State the blood parasite species.
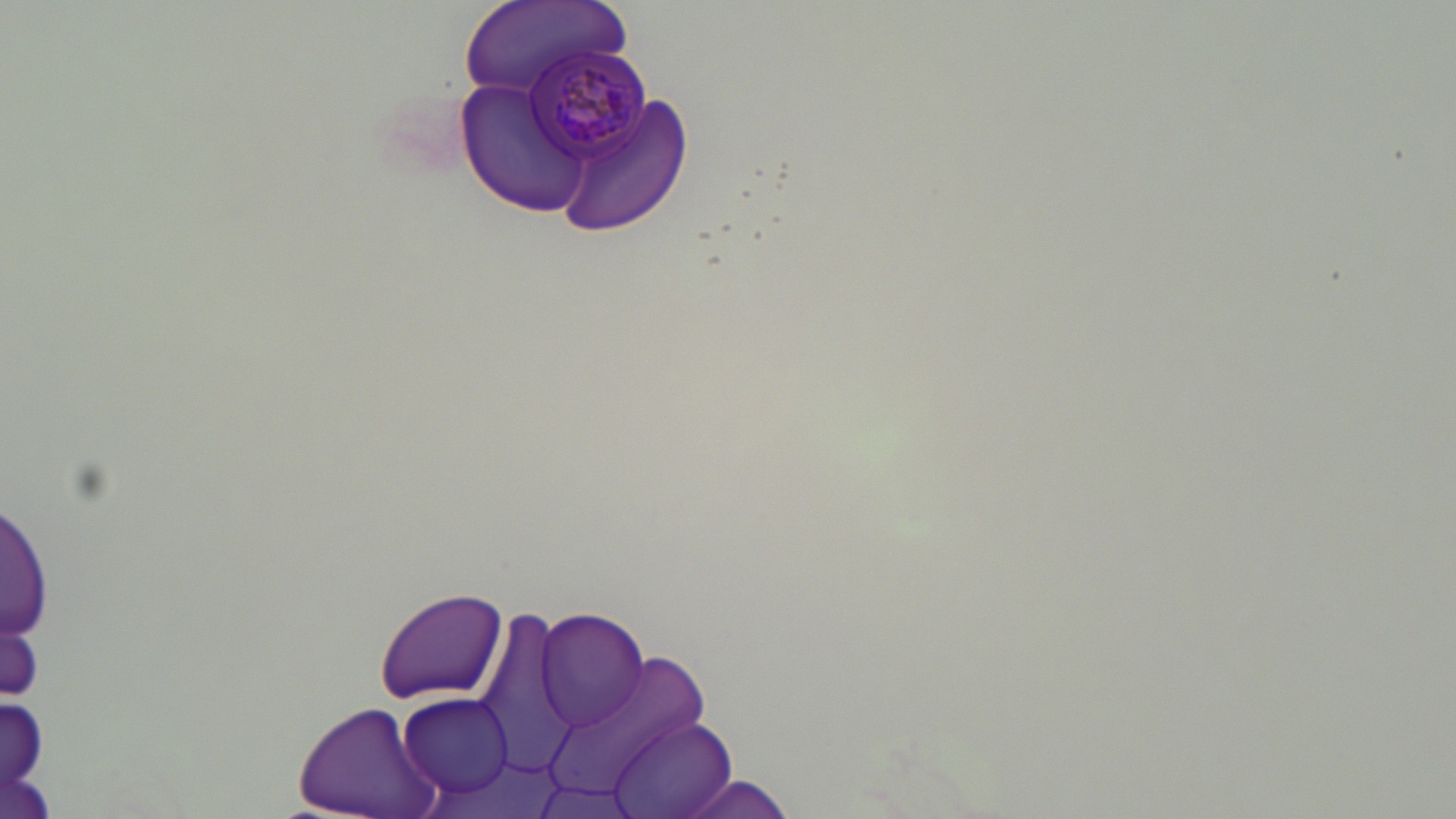
Plasmodium malariae.

uninfected red blood cell locations = approximate bounding boxes as (x1, y1, x2, y2) in pixels: (458, 0, 629, 105), (454, 76, 600, 218), (552, 91, 695, 239), (1, 499, 50, 650), (373, 587, 509, 703), (468, 600, 584, 778), (536, 608, 651, 733), (547, 654, 709, 802), (397, 692, 518, 801), (293, 699, 442, 819), (606, 716, 736, 819), (678, 776, 803, 819)
stain = May-Grünwald-Giemsa
magnification = 1000x
preparation = thin blood smear
field of view = single
image size = 1456×819 pixels
modality = light microscopy
Plasmodium malariae-infected red blood cell locations = approximate bounding boxes as (x1, y1, x2, y2) in pixels: (526, 47, 654, 166)